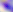

400x magnification. Toxoplasma gondii is shown. Micrograph.